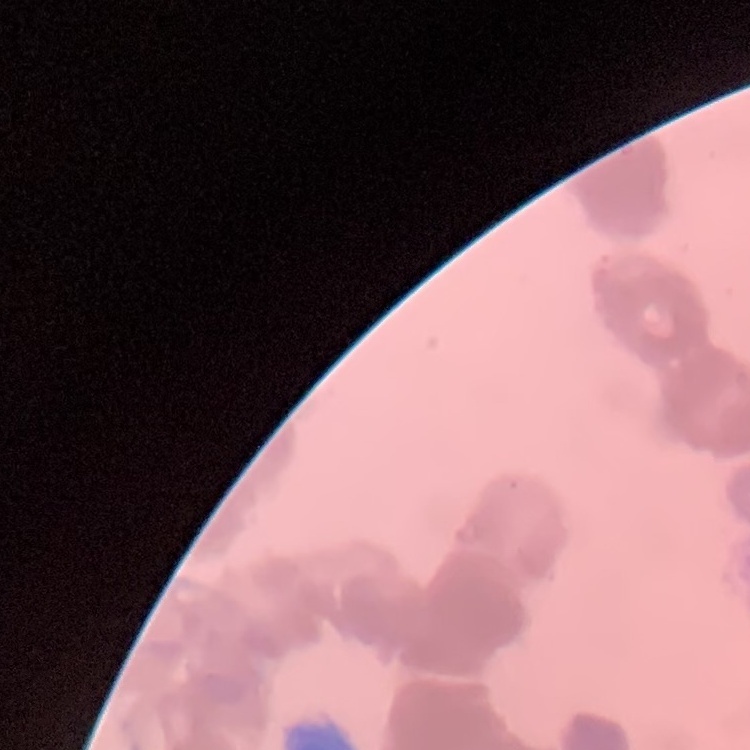

red blood cell morphology = rouleaux formation
stain = Field's or Giemsa
preparation = thin blood smear
image type = square crop of a larger photomicrograph